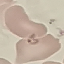
result = malaria parasites identified
preparation = thin blood film
stain = Giemsa
image type = cell patch, automatically extracted from a larger field of view and resized to 64 × 64 pixels
capture = smartphone camera at the microscope eyepiece